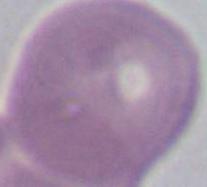
Photomicrograph. Captured at 1000x magnification. An erythrocyte is shown.